Assess the morphology of the red blood cells.
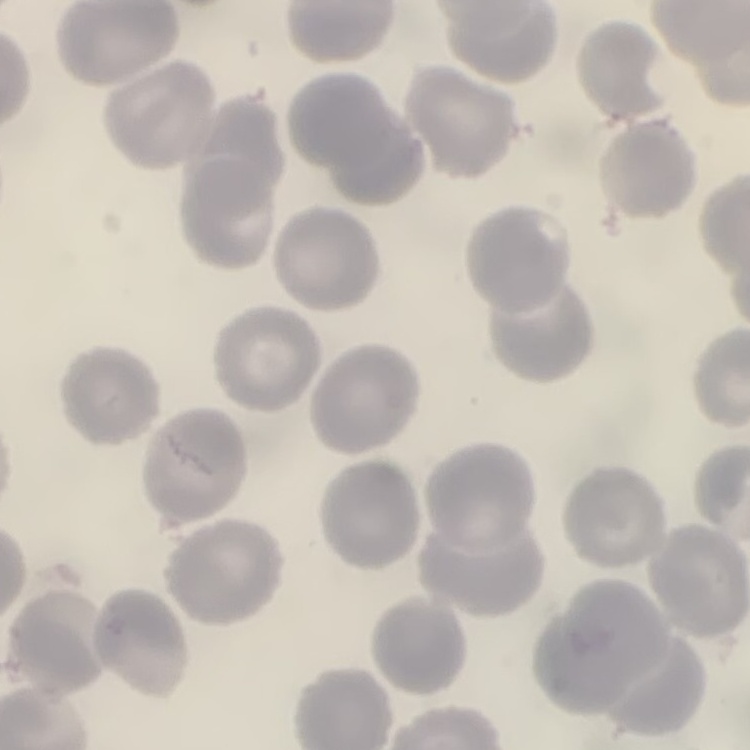
They show no rouleaux formation.

Summary:
  - Stain: Field's or Giemsa
  - Preparation: thin blood film
  - Image type: one tile cut from a larger photomicrograph